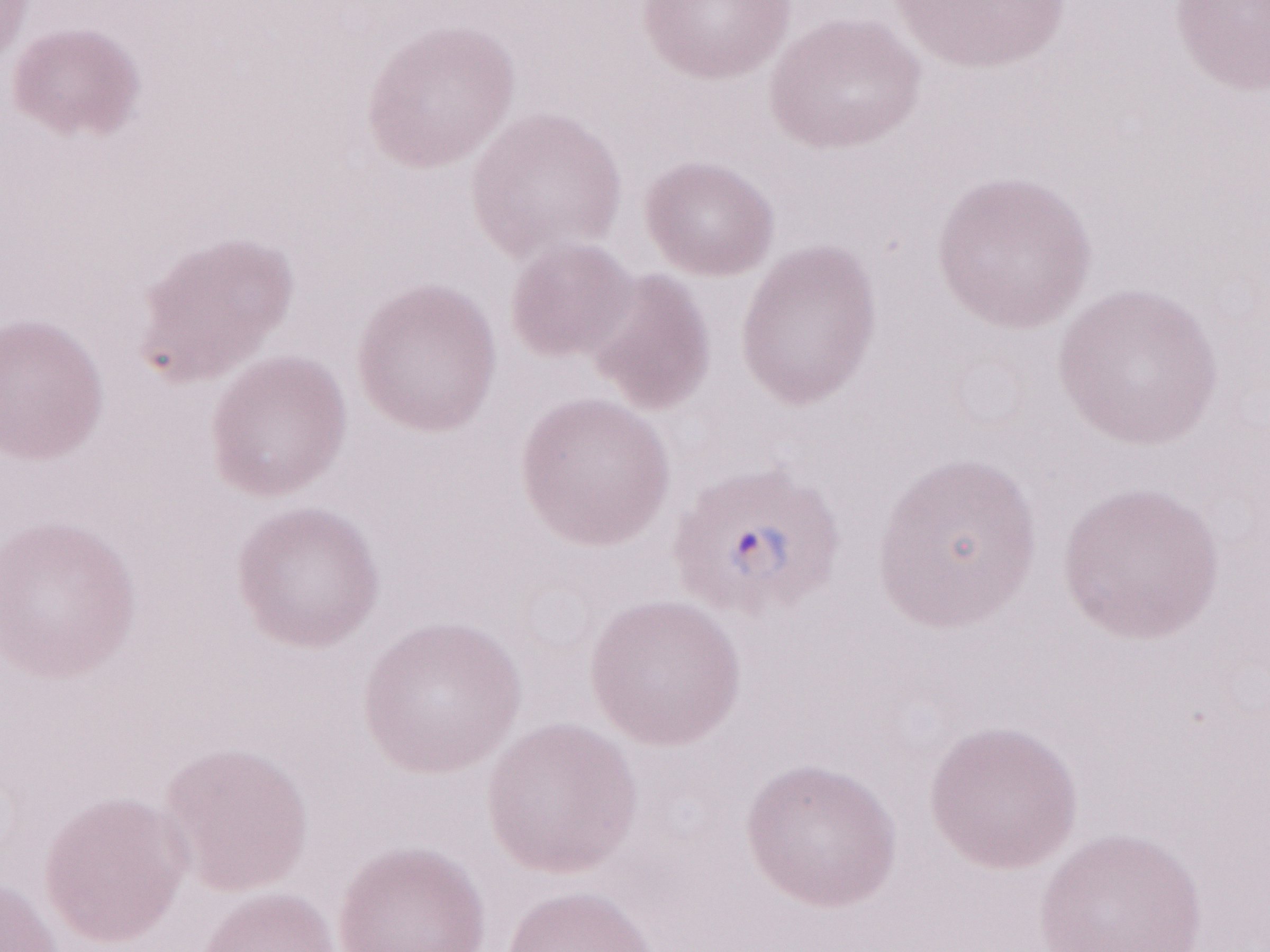

Thin blood film. Olympus BX43 microscope and DP73 digital camera. May-Grünwald-Giemsa stain. Image is 1270×952 pixels. Magnification: 1,000x. Malaria diagnosis (patient-level): positive. Single field of view.